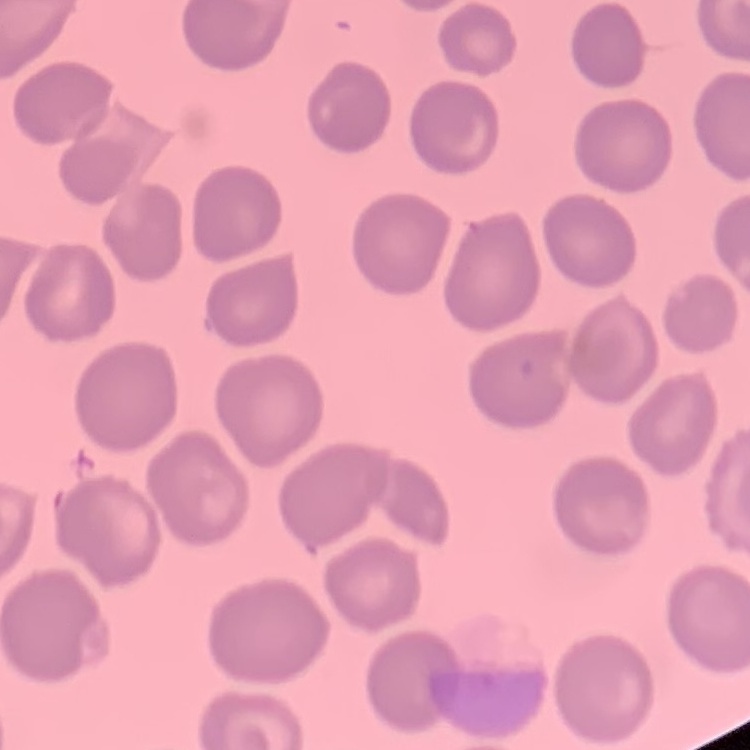
{
  "red_blood_cell_morphology": "no rouleaux formation",
  "image_type": "square crop of a larger photomicrograph",
  "stain": "Field's or Giemsa",
  "preparation": "thin blood film"
}